Identify the cell.
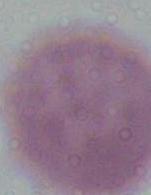
This is an erythrocyte.

{
  "magnification": "1000x",
  "modality": "micrograph"
}